Comment on the morphology of the erythrocytes.
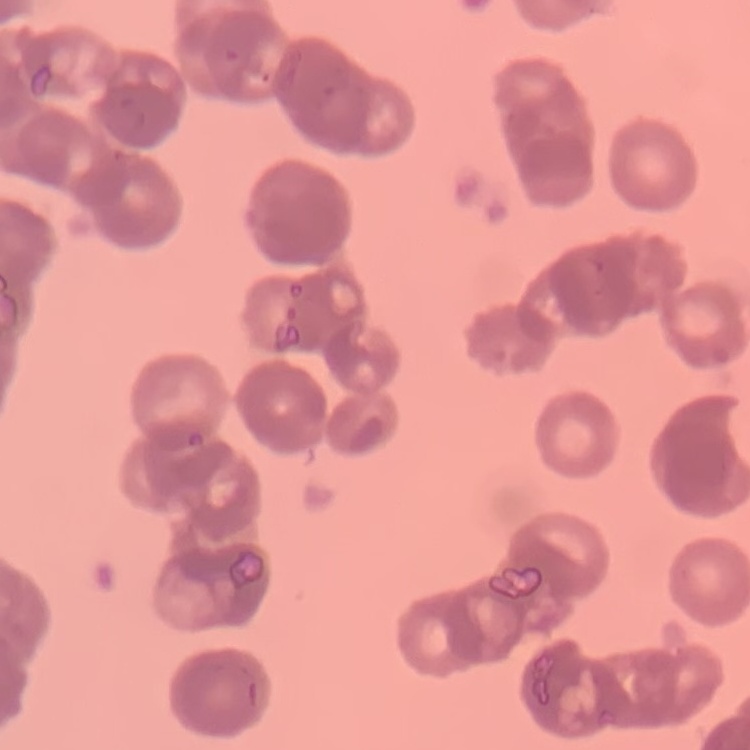
Rouleaux formation.

Summary:
  - Stain: Field's or Giemsa
  - Image type: square crop of a larger photomicrograph
  - Preparation: thin blood film